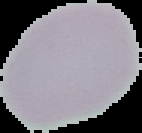 Result: no Plasmodium parasites seen. From a thin blood smear. Segmented cell region on a black background. Image is 142×133 pixels.